Outline each Plasmodium vivax-infected red blood cell.
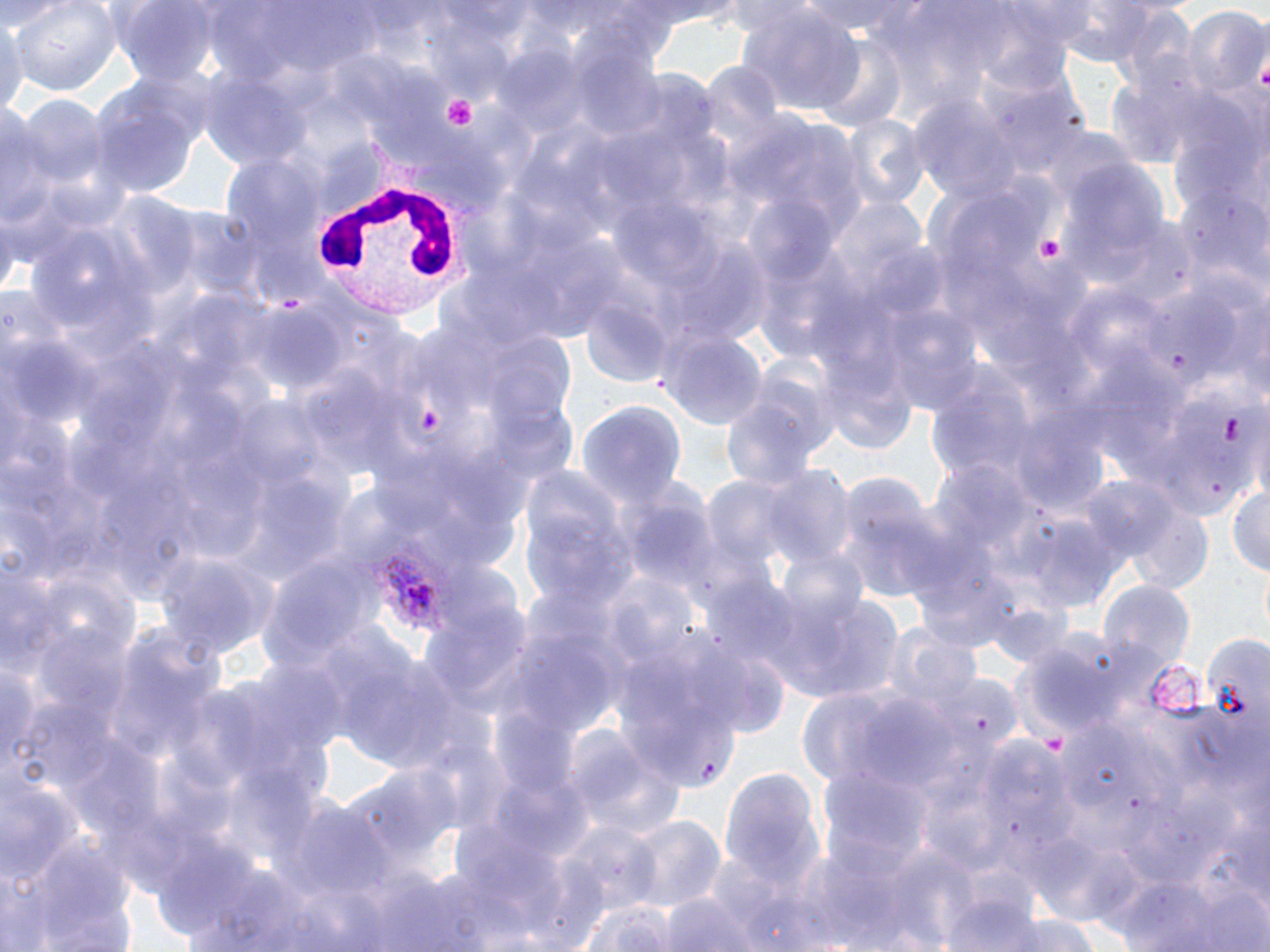
Approximate bounding boxes as [x1, y1, x2, y2] in pixels.
Plasmodium vivax-infected red blood cells: [347, 535, 459, 639].

White blood cell locations: [315, 141, 479, 333]. Uninfected red blood cell locations: [8, 0, 122, 97], [111, 0, 223, 90], [797, 0, 931, 39], [736, 5, 867, 118], [1183, 10, 1270, 100], [0, 12, 25, 127], [816, 39, 908, 134], [202, 71, 317, 171], [88, 82, 205, 199], [17, 96, 106, 187], [912, 99, 1019, 202], [0, 101, 47, 234], [839, 115, 928, 212], [103, 196, 198, 295], [831, 198, 930, 294], [1103, 218, 1198, 309], [578, 298, 674, 390], [659, 326, 768, 431], [922, 365, 1043, 509], [718, 386, 827, 497], [577, 404, 685, 515], [512, 460, 636, 607], [833, 469, 949, 602], [1081, 474, 1188, 568], [1227, 484, 1269, 581], [1121, 502, 1216, 594], [1022, 516, 1127, 613], [153, 544, 274, 664], [1100, 582, 1194, 671], [767, 591, 903, 704], [98, 624, 224, 766], [881, 627, 985, 721], [1197, 639, 1270, 729], [341, 653, 468, 771], [2, 660, 44, 771], [569, 732, 686, 841], [716, 767, 824, 890], [0, 782, 83, 889], [269, 795, 395, 902], [622, 817, 726, 917], [9, 830, 139, 952], [941, 876, 1046, 952], [658, 892, 763, 952], [579, 899, 677, 951], [992, 913, 1103, 952]. Platelet locations: [443, 95, 477, 130], [1036, 236, 1067, 264]. Slide-level diagnosis: Plasmodium vivax. Image is 1270×952 pixels. Single field of view. Thin blood film. Light microscopy. Captured at 1000x magnification. May-Grünwald-Giemsa-stained preparation.